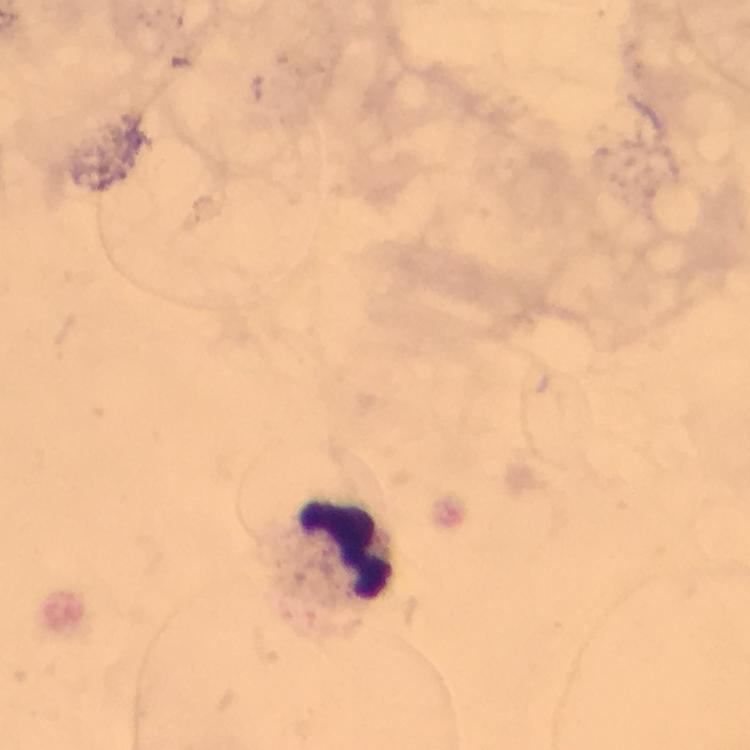

Approximate centers as [x, y] in pixels. Leukocyte locations: [345, 548]. Immersion oil applied. Giemsa stain. Smartphone photograph taken through a microscope. A crop from one field of view. From a malaria diagnostic workup. Plasmodium parasites: none detected. Image is 750×750 pixels. At 100x magnification. Thick blood smear.